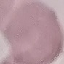
result = no malaria parasites seen
stain = Giemsa
image type = automatically extracted cell patch, resized to 64 × 64 pixels
capture = smartphone camera at the microscope eyepiece
preparation = thin blood smear